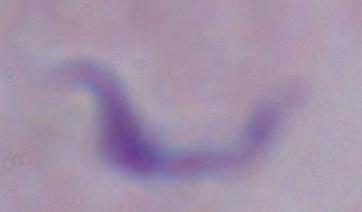

identification = trypanosome
magnification = 1000x
modality = photomicrograph